Comment on the morphology of the red blood cells.
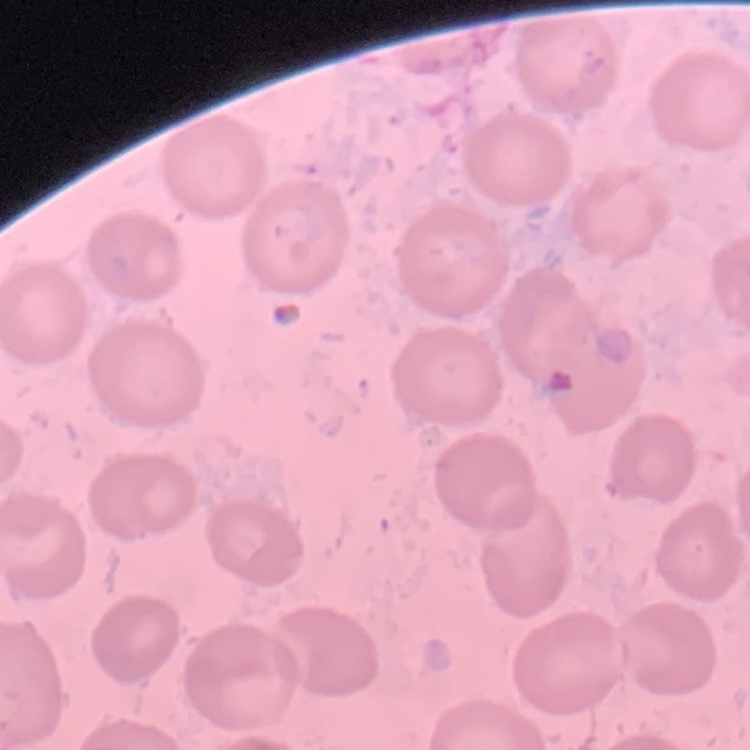
They show no rouleaux formation.

Stained with either Field's or Giemsa. Square crop of a larger photomicrograph. Thin peripheral smear.